Name the blood parasite species.
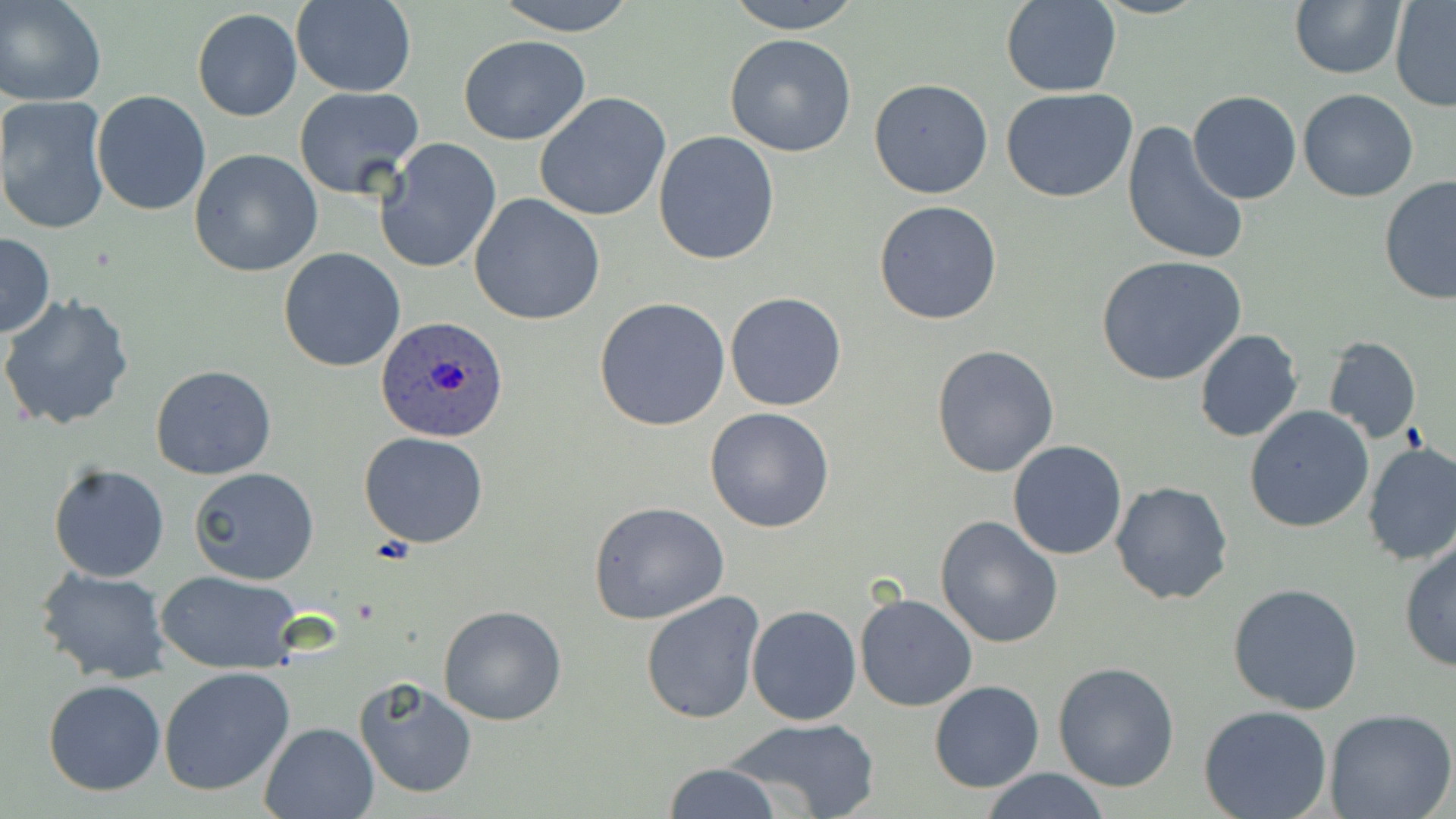
Plasmodium ovale.

Summary:
  - Coordinate format: approximate bounding boxes as (x1,y1)-(x2,y2) corner pairs in pixels
  - Plasmodium ovale-infected red blood cell locations: (376,316)-(510,444)
  - Uninfected red blood cell locations: (1,0)-(107,106), (290,0)-(417,97), (491,0)-(641,36), (724,0)-(862,33), (1290,0)-(1406,79), (1390,0)-(1456,111), (1001,1)-(1123,98), (191,8)-(303,122), (724,34)-(857,157), (459,35)-(590,145), (868,78)-(993,200), (294,86)-(425,200), (1000,87)-(1138,202), (1297,88)-(1418,202), (1188,90)-(1302,205), (92,91)-(212,215), (534,92)-(670,222), (0,95)-(110,235), (1121,121)-(1250,268), (652,132)-(780,265), (375,138)-(502,274), (189,148)-(323,278), (1378,175)-(1456,307), (469,193)-(606,326), (873,199)-(1003,325), (0,233)-(56,337), (278,247)-(405,372), (1098,256)-(1247,388), (724,291)-(847,412), (0,293)-(135,433), (595,296)-(730,431), (1194,330)-(1304,443), (1321,335)-(1421,442), (931,345)-(1060,477), (149,365)-(276,481), (1244,405)-(1375,533), (703,408)-(835,533), (359,432)-(490,548), (1007,441)-(1127,559), (1362,443)-(1456,567), (47,463)-(171,583), (188,467)-(320,585), (1110,482)-(1233,605), (587,501)-(732,624), (934,514)-(1064,649), (1399,538)-(1455,672), (32,566)-(171,683), (156,570)-(305,673), (1228,583)-(1363,716), (640,591)-(765,724), (854,592)-(977,711), (746,604)-(862,725), (437,605)-(567,726), (1053,662)-(1180,792), (159,666)-(296,797), (355,676)-(478,799), (43,680)-(165,796), (928,680)-(1045,792), (1197,703)-(1333,819), (1322,706)-(1454,819), (721,716)-(880,819), (259,721)-(380,818), (660,762)-(786,819), (976,768)-(1112,819)
  - Field of view: one of a larger specimen
  - Modality: optical microscopy
  - Preparation: thin blood film
  - Magnification: 1000x
  - Image size: 1456×819 pixels
  - Stain: May-Grünwald-Giemsa